Report the malaria status of this cell.
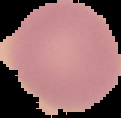

It is uninfected.

Summary:
  - Preparation: thin blood film
  - Image size: 121×118 pixels
  - Image type: segmented cell region on a black background